Name the parasite shown.
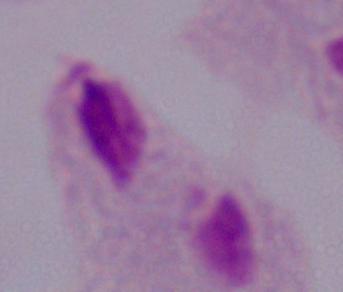

A trichomonad.

magnification = 1000x
modality = photomicrograph